Name the parasite shown.
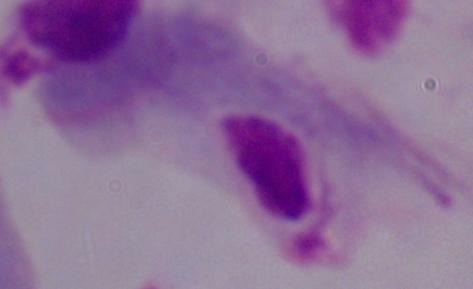
This is a trichomonad.

modality = photomicrograph
magnification = 1000x